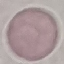
Malaria status: uninfected. Photographed with a smartphone camera at the microscope eyepiece. Cell patch, automatically extracted from a larger field of view and resized to 64 × 64 pixels. Thin blood film. Giemsa stain.